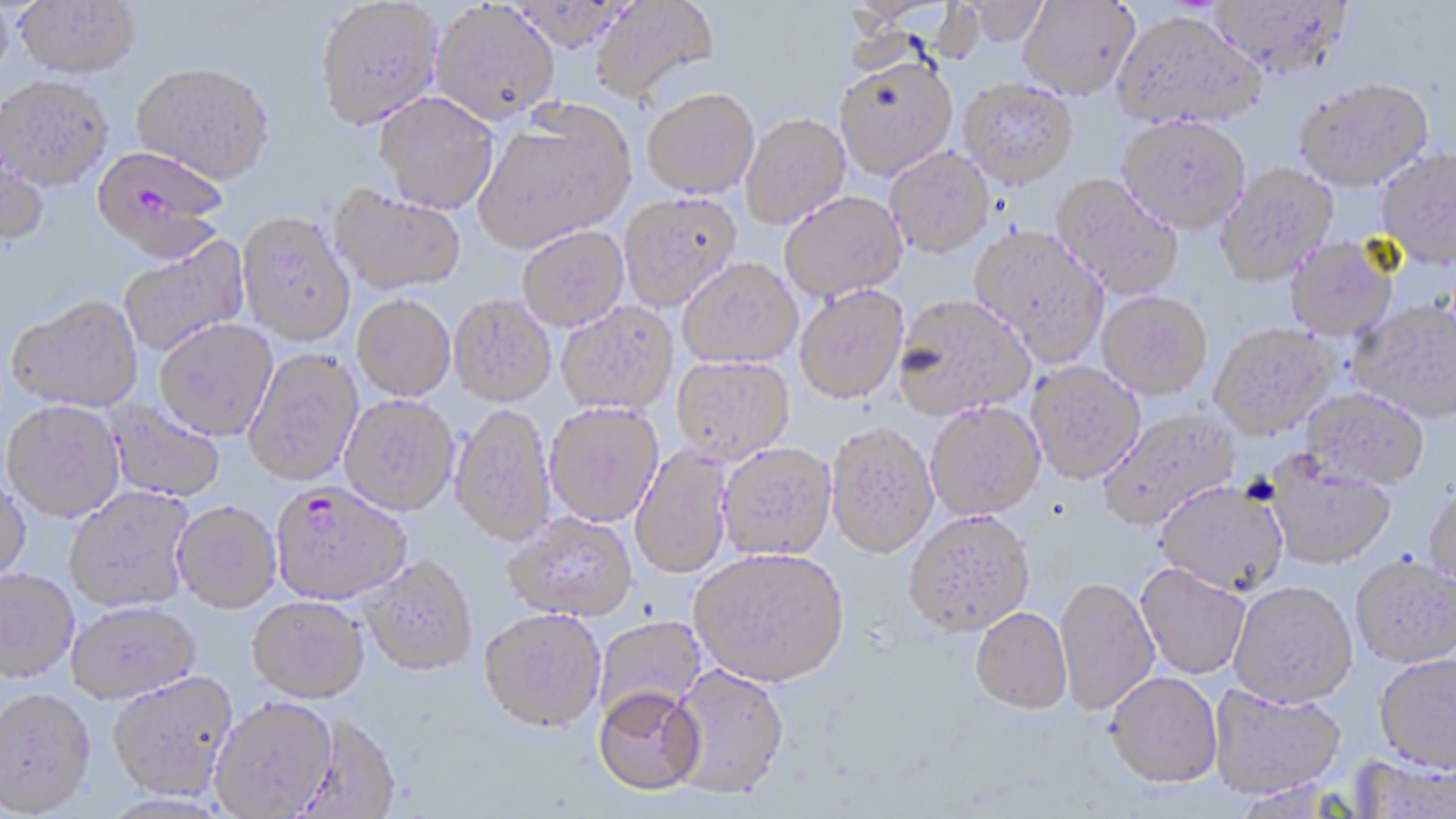
Plasmodium falciparum-infected red blood cell locations = approximate bounding boxes as [x1, y1, x2, y2] in pixels: [91, 148, 226, 264], [270, 483, 410, 606]
slide-level diagnosis = Plasmodium falciparum
field of view = one of a larger specimen
modality = optical microscopy
magnification = 1000x
image size = 1456×819 pixels
uninfected red blood cell locations = approximate bounding boxes as [x1, y1, x2, y2] in pixels: [590, 0, 720, 105], [959, 0, 1050, 47], [1019, 0, 1139, 99], [1209, 0, 1354, 79], [0, 1, 14, 90], [14, 1, 141, 84], [315, 2, 442, 133], [431, 3, 559, 126], [1112, 11, 1265, 130], [834, 53, 958, 179], [132, 66, 273, 188], [958, 78, 1079, 188], [0, 79, 113, 194], [1295, 81, 1434, 192], [642, 88, 759, 198], [374, 93, 499, 215], [474, 103, 636, 253], [740, 113, 851, 229], [1119, 115, 1250, 232], [0, 125, 49, 250], [886, 147, 995, 257], [1376, 151, 1456, 270], [1216, 163, 1338, 286], [1052, 174, 1183, 300], [328, 185, 465, 296], [779, 191, 907, 302], [619, 192, 742, 310], [237, 214, 355, 348], [518, 226, 629, 330], [970, 226, 1109, 365], [118, 233, 250, 358], [1285, 237, 1397, 341], [677, 257, 802, 368], [794, 284, 909, 403], [1097, 291, 1212, 398], [893, 294, 1036, 419], [352, 295, 455, 401], [449, 295, 556, 407], [6, 298, 143, 415], [1350, 301, 1456, 422], [556, 302, 678, 415], [154, 321, 277, 442], [1209, 323, 1338, 439], [243, 349, 363, 487], [671, 355, 796, 465], [1027, 362, 1145, 484], [1301, 388, 1429, 489], [339, 395, 459, 516], [104, 397, 226, 503], [925, 401, 1044, 519], [2, 402, 125, 523], [545, 402, 664, 526], [450, 404, 556, 548], [1099, 407, 1240, 530], [826, 421, 938, 558], [717, 442, 836, 560], [630, 445, 733, 579], [1265, 452, 1396, 569], [0, 476, 31, 590], [1156, 481, 1288, 594], [1423, 485, 1456, 592], [64, 488, 194, 613], [173, 503, 281, 614], [903, 509, 1035, 635], [504, 513, 636, 622], [689, 546, 850, 686], [1351, 555, 1456, 667], [359, 556, 477, 677], [1136, 564, 1250, 679], [0, 569, 79, 683], [1055, 576, 1159, 715], [1229, 580, 1358, 706], [246, 597, 369, 704], [67, 603, 201, 704], [971, 607, 1072, 713], [479, 608, 606, 732], [595, 616, 706, 723], [1373, 653, 1456, 772], [667, 663, 791, 799], [1106, 671, 1222, 786], [107, 673, 238, 802], [1209, 684, 1345, 798], [593, 686, 705, 796], [0, 689, 96, 817], [210, 698, 337, 818], [293, 714, 401, 817], [1350, 752, 1454, 818]
preparation = thin blood smear
stain = May-Grünwald-Giemsa